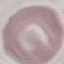
malaria status = uninfected
image type = automatically extracted cell patch, resized to 64 × 64 pixels
preparation = thin smear
stain = Giemsa
capture = smartphone camera at the microscope eyepiece